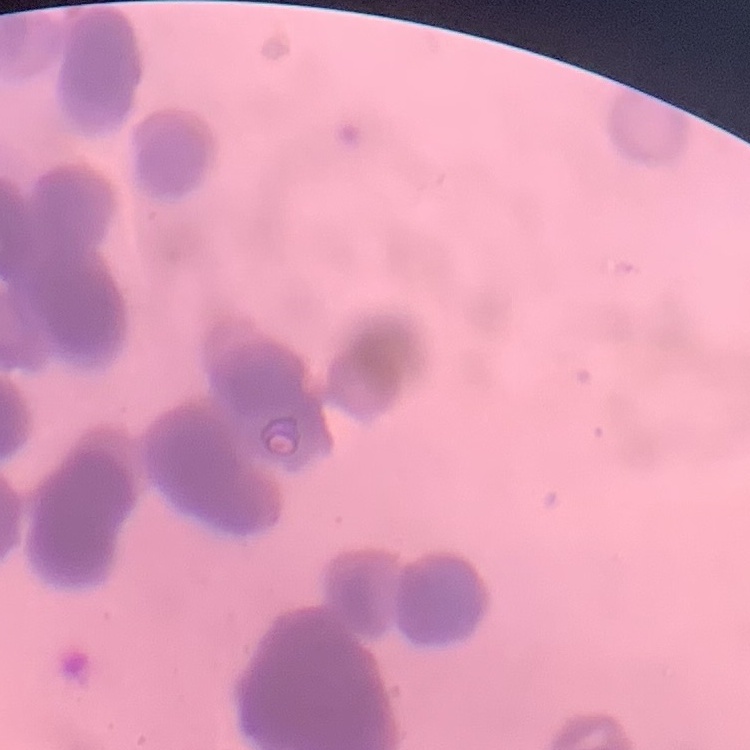
The erythrocytes exhibit rouleaux formation. Square crop of a larger photomicrograph. Thin peripheral smear. Stained with either Field's or Giemsa.